Outline platelets.
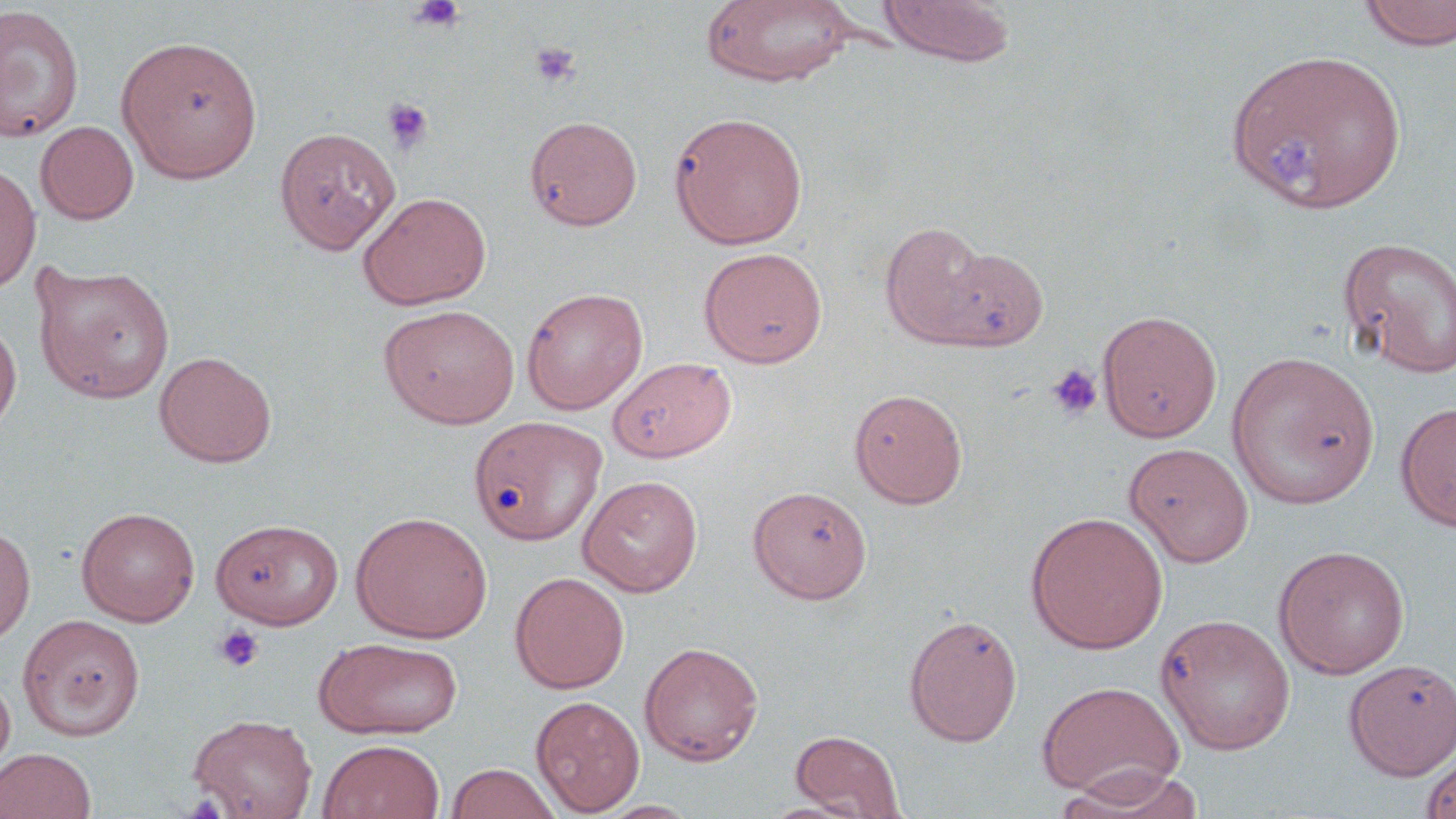
Approximate bounding boxes as named x1/y1/x2/y2 corners in pixels.
Platelets: (x1=407, y1=0, x2=467, y2=34), (x1=529, y1=41, x2=582, y2=90), (x1=381, y1=98, x2=434, y2=154), (x1=1272, y1=136, x2=1323, y2=186), (x1=1046, y1=363, x2=1103, y2=420), (x1=213, y1=624, x2=264, y2=673).

Uninfected red blood cell locations: (x1=877, y1=0, x2=1015, y2=66), (x1=1358, y1=0, x2=1456, y2=50), (x1=702, y1=1, x2=857, y2=88), (x1=0, y1=5, x2=84, y2=143), (x1=116, y1=35, x2=263, y2=183), (x1=1224, y1=46, x2=1408, y2=214), (x1=669, y1=111, x2=809, y2=249), (x1=525, y1=116, x2=643, y2=230), (x1=35, y1=120, x2=139, y2=224), (x1=274, y1=126, x2=401, y2=254), (x1=0, y1=162, x2=41, y2=293), (x1=357, y1=191, x2=492, y2=309), (x1=880, y1=221, x2=996, y2=345), (x1=1338, y1=236, x2=1456, y2=378), (x1=931, y1=245, x2=1050, y2=350), (x1=698, y1=246, x2=828, y2=368), (x1=32, y1=261, x2=175, y2=404), (x1=521, y1=287, x2=648, y2=415), (x1=380, y1=303, x2=520, y2=428), (x1=1097, y1=309, x2=1222, y2=443), (x1=0, y1=320, x2=22, y2=435), (x1=154, y1=351, x2=277, y2=468), (x1=1226, y1=351, x2=1380, y2=509), (x1=607, y1=356, x2=737, y2=462), (x1=849, y1=387, x2=968, y2=508), (x1=1395, y1=401, x2=1456, y2=533), (x1=469, y1=416, x2=606, y2=546), (x1=1123, y1=442, x2=1255, y2=567), (x1=578, y1=475, x2=703, y2=597), (x1=748, y1=485, x2=873, y2=603), (x1=76, y1=506, x2=200, y2=626), (x1=350, y1=510, x2=493, y2=643), (x1=1025, y1=511, x2=1169, y2=654), (x1=210, y1=518, x2=343, y2=629), (x1=0, y1=521, x2=36, y2=648), (x1=1273, y1=544, x2=1410, y2=679), (x1=509, y1=571, x2=630, y2=694), (x1=1155, y1=613, x2=1296, y2=755), (x1=18, y1=614, x2=144, y2=740), (x1=904, y1=614, x2=1022, y2=746), (x1=313, y1=637, x2=464, y2=739), (x1=639, y1=641, x2=764, y2=766), (x1=1344, y1=659, x2=1456, y2=780), (x1=0, y1=671, x2=15, y2=777), (x1=1036, y1=680, x2=1184, y2=800), (x1=530, y1=695, x2=645, y2=815), (x1=187, y1=713, x2=318, y2=819), (x1=789, y1=730, x2=907, y2=818), (x1=317, y1=738, x2=445, y2=819), (x1=0, y1=747, x2=97, y2=819), (x1=1420, y1=750, x2=1456, y2=819), (x1=445, y1=763, x2=562, y2=819), (x1=1053, y1=765, x2=1208, y2=818), (x1=594, y1=799, x2=703, y2=818). Slide-level diagnosis: no evidence of blood parasites. May-Grünwald-Giemsa-stained preparation. 1000x magnification. Thin blood smear. Image is 1456×819 pixels. One field of a larger specimen. Optical microscopy.